Comment on the morphology of the erythrocytes.
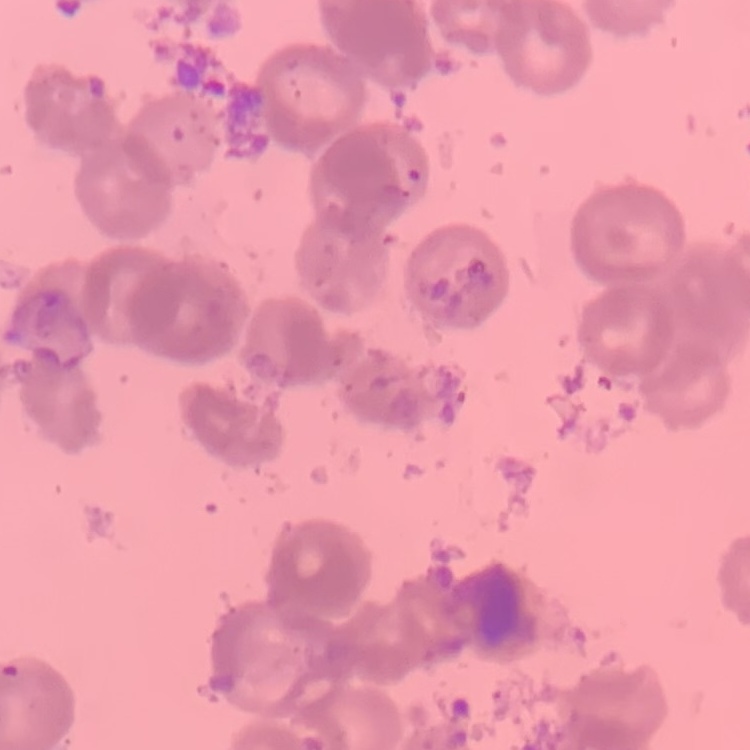
Rouleaux formation.

Thin peripheral smear. One tile cut from a larger photomicrograph. Stained with either Field's or Giemsa.